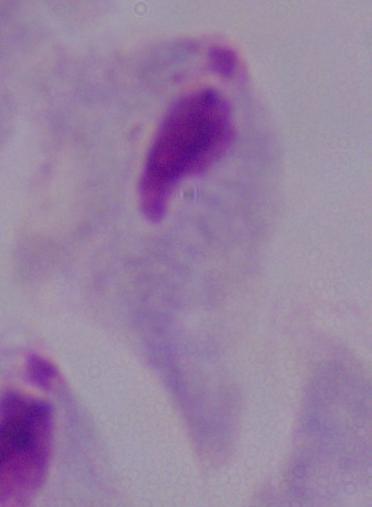

Captured at 1000x magnification. A trichomonad is shown. Micrograph.